Locate and identify every blood parasite.
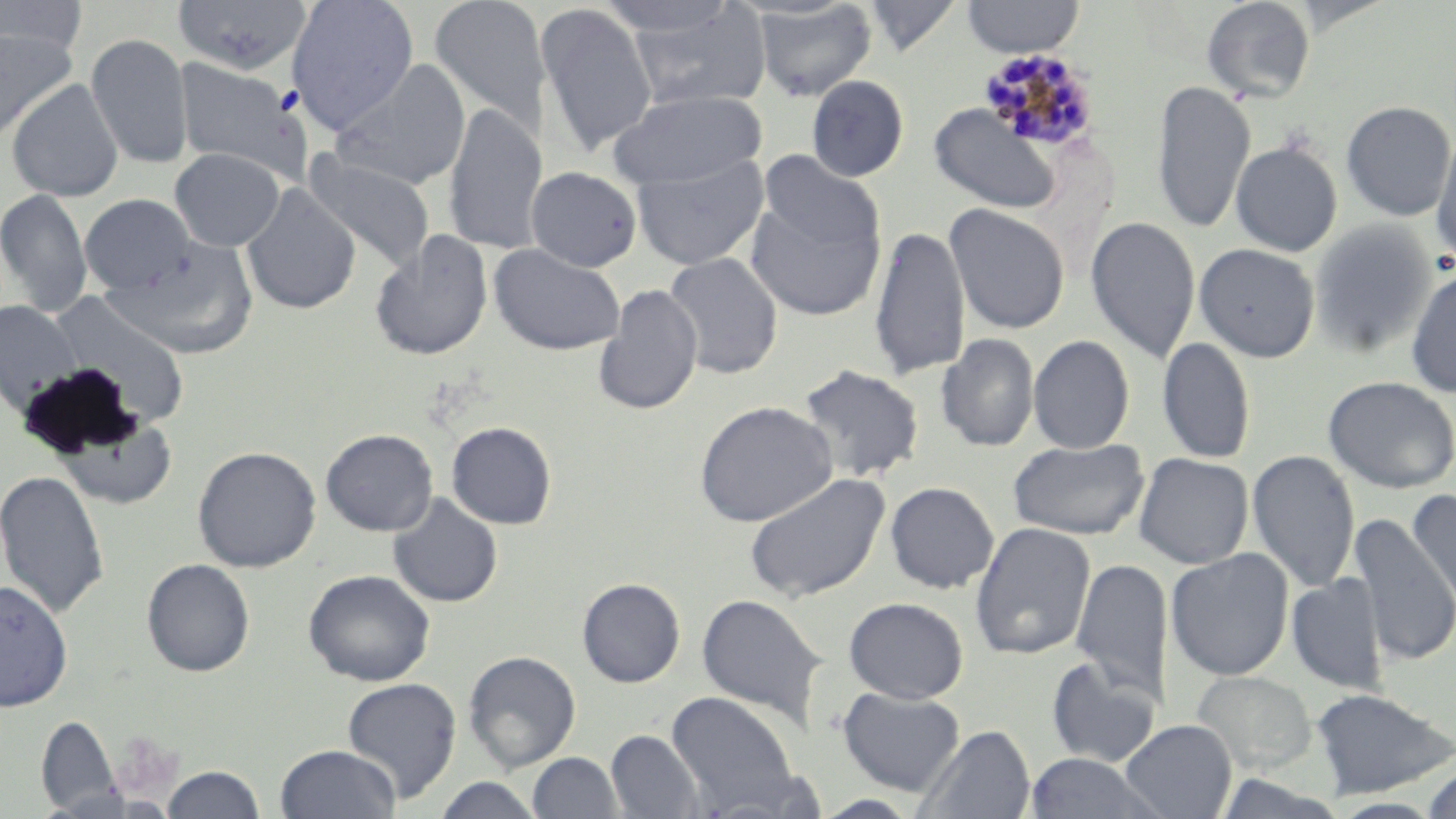

Approximate bounding boxes as [x1, y1, x2, y2] in pixels.
Plasmodium malariae-infected red blood cells: [980, 48, 1101, 153].
No Plasmodium falciparum, Plasmodium ovale, Plasmodium vivax, Babesia divergens, or Trypanosoma brucei observed.

Uninfected red blood cell locations: [0, 0, 88, 57], [172, 0, 313, 75], [286, 0, 419, 134], [429, 0, 551, 140], [863, 0, 963, 57], [961, 0, 1086, 58], [1201, 0, 1316, 103], [751, 1, 877, 102], [622, 2, 772, 112], [535, 3, 658, 157], [1, 28, 77, 143], [86, 33, 194, 170], [173, 57, 308, 182], [329, 59, 471, 192], [806, 74, 909, 182], [6, 78, 124, 202], [1152, 80, 1254, 235], [608, 89, 767, 190], [1340, 100, 1456, 221], [443, 103, 545, 255], [930, 105, 1060, 214], [1432, 128, 1456, 268], [1230, 140, 1343, 256], [170, 148, 286, 251], [758, 150, 885, 259], [303, 152, 436, 270], [631, 154, 770, 271], [525, 166, 643, 272], [241, 182, 361, 315], [0, 187, 93, 318], [743, 190, 884, 322], [79, 193, 195, 296], [944, 203, 1071, 334], [1085, 215, 1201, 364], [1309, 221, 1436, 359], [870, 224, 970, 381], [368, 230, 494, 361], [108, 241, 260, 359], [489, 243, 626, 355], [1194, 243, 1320, 362], [663, 252, 783, 379], [1405, 264, 1456, 399], [594, 283, 703, 416], [48, 291, 191, 429], [0, 300, 83, 416], [936, 333, 1039, 452], [1028, 335, 1134, 454], [1157, 337, 1256, 464], [797, 363, 924, 483], [1322, 376, 1456, 493], [694, 400, 838, 527], [54, 417, 181, 508], [446, 422, 557, 529], [320, 428, 438, 536], [1008, 437, 1150, 541], [192, 445, 322, 573], [1247, 450, 1360, 592], [1133, 452, 1254, 569], [0, 469, 109, 618], [744, 471, 891, 603], [885, 481, 999, 594], [1406, 488, 1456, 612], [388, 493, 503, 608], [1350, 514, 1455, 666], [969, 522, 1096, 661], [1165, 548, 1295, 680], [141, 558, 255, 676], [1071, 558, 1172, 700], [303, 569, 435, 686], [1287, 574, 1388, 694], [577, 577, 686, 687], [0, 578, 73, 712], [696, 593, 827, 729], [844, 597, 968, 703], [463, 650, 581, 772], [1045, 656, 1162, 768], [1190, 671, 1317, 774], [342, 677, 461, 803], [837, 686, 966, 796], [1309, 687, 1455, 799], [666, 691, 798, 811], [36, 715, 122, 815], [1119, 719, 1237, 819], [915, 724, 1036, 818], [607, 729, 704, 819], [274, 744, 401, 819], [1023, 751, 1162, 818], [527, 752, 623, 818], [162, 764, 265, 818], [1422, 768, 1456, 819], [1212, 773, 1346, 817], [430, 776, 546, 818], [812, 794, 922, 818]. Slide-level diagnosis: Plasmodium malariae. 1000x magnification. Light microscopy. Thin blood smear. May-Grünwald-Giemsa-stained preparation. Image is 1456×819 pixels. Single field of view.